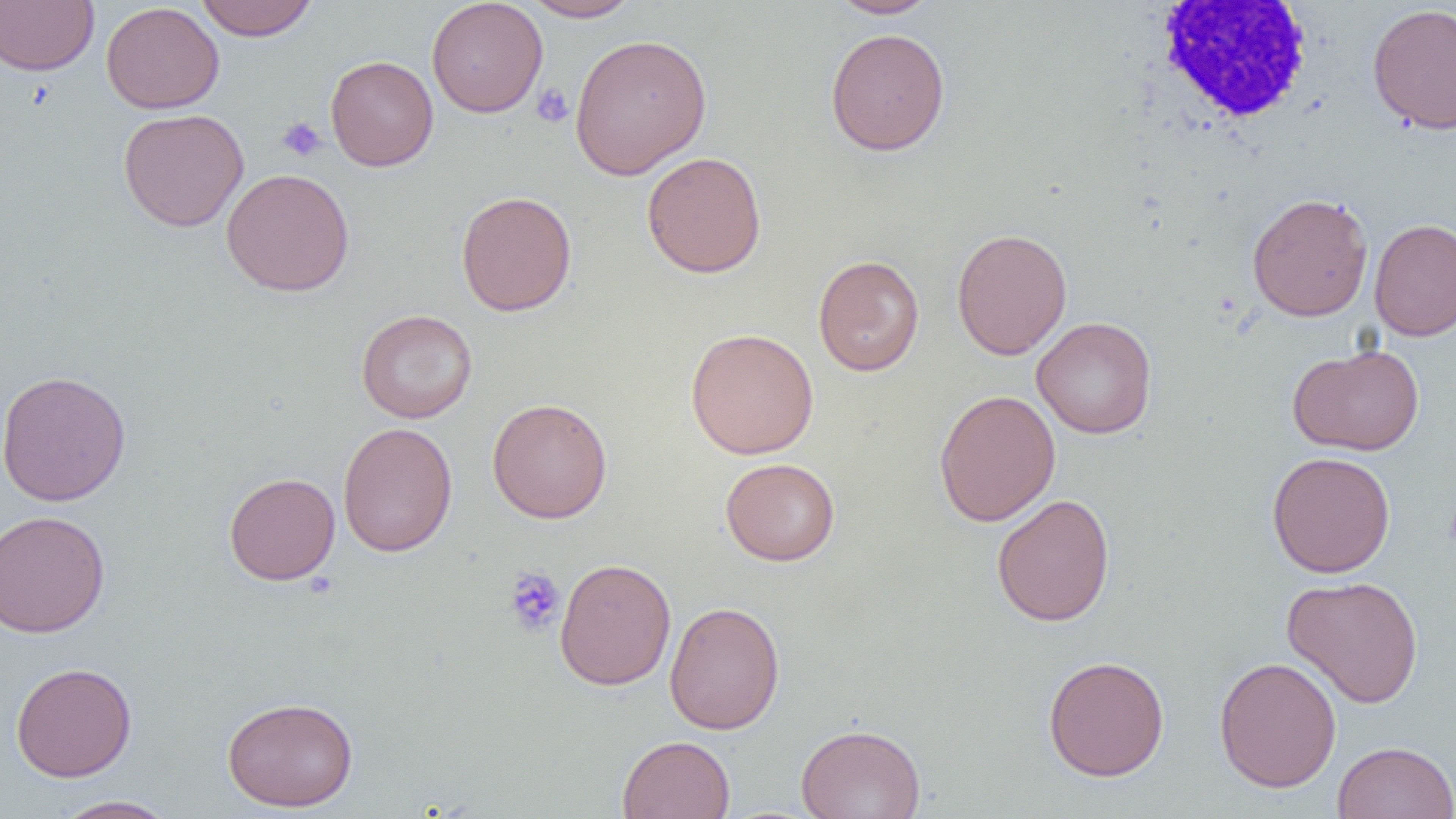

slide-level diagnosis = no evidence of blood parasites
preparation = thin blood film
white blood cell locations = approximate bounding boxes as [x1, y1, x2, y2] in pixels: [1145, 2, 1319, 130]
magnification = 1000x
field of view = one of a larger specimen
image size = 1456×819 pixels
platelet locations = approximate bounding boxes as [x1, y1, x2, y2] in pixels: [531, 83, 574, 128], [277, 116, 327, 162], [503, 566, 566, 637]
uninfected red blood cell locations = approximate bounding boxes as [x1, y1, x2, y2] in pixels: [195, 0, 319, 41], [522, 0, 642, 22], [826, 0, 941, 19], [0, 1, 98, 76], [426, 1, 548, 117], [100, 2, 225, 114], [1367, 3, 1456, 136], [825, 27, 951, 156], [569, 33, 712, 180], [325, 54, 438, 171], [118, 108, 249, 232], [641, 151, 767, 278], [221, 168, 355, 296], [456, 190, 577, 317], [1247, 192, 1373, 322], [1369, 218, 1456, 341], [951, 227, 1072, 360], [812, 254, 925, 376], [356, 308, 477, 423], [1032, 316, 1158, 439], [685, 327, 819, 459], [1287, 342, 1424, 456], [0, 369, 131, 507], [933, 388, 1061, 527], [487, 398, 612, 523], [337, 422, 457, 557], [1266, 451, 1396, 578], [720, 457, 840, 566], [224, 472, 340, 585], [991, 494, 1115, 626], [0, 510, 110, 638], [555, 558, 676, 691], [1282, 575, 1424, 708], [664, 601, 785, 734], [1042, 654, 1170, 782], [1213, 656, 1342, 792], [10, 661, 137, 782], [221, 696, 359, 811], [795, 722, 926, 819], [617, 734, 735, 819], [1332, 741, 1456, 819], [52, 795, 178, 819]
modality = light microscopy